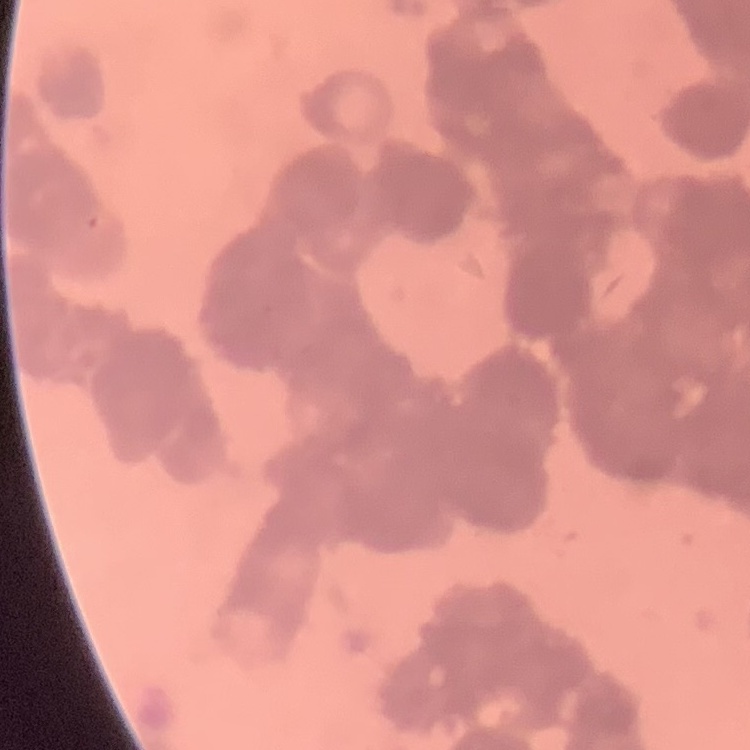

The erythrocytes show rouleaux formation. Thin blood smear. Field's or Giemsa stain. Square crop of a larger photomicrograph.